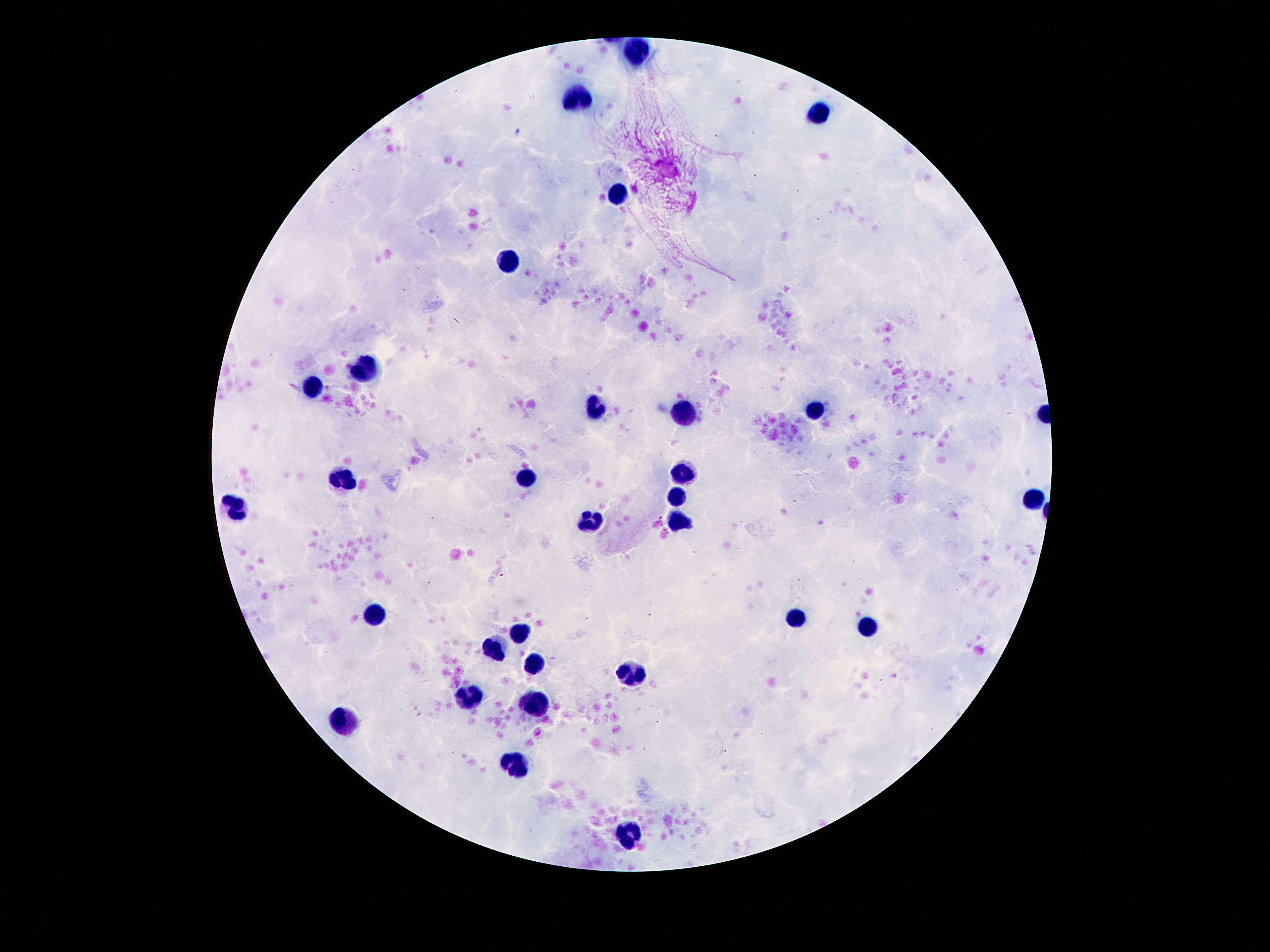

magnification = 100x
stain = Giemsa
field of view = one from this slide
leukocyte locations = approximate centers as [x, y] in pixels: [641, 51], [577, 99], [818, 113], [617, 195], [507, 259], [363, 369], [314, 386], [594, 408], [816, 411], [686, 415], [682, 475], [344, 479], [525, 479], [675, 497], [1031, 501], [232, 508], [591, 518], [675, 520], [376, 611], [794, 616], [869, 628], [518, 634], [495, 645], [533, 666], [628, 677], [469, 693], [536, 705], [340, 720], [516, 766], [630, 833]
preparation = thick blood film
image size = 1270×952 pixels
patient malaria status = negative
capture = smartphone camera through the microscope eyepiece